Report the malaria status of this cell.
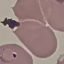

It is parasitized.

Thin blood film. Acquired by smartphone through the microscope eyepiece. Giemsa stain. Cell patch, automatically extracted from a larger field of view and resized to 64 × 64 pixels.